Locate every Plasmodium parasite.
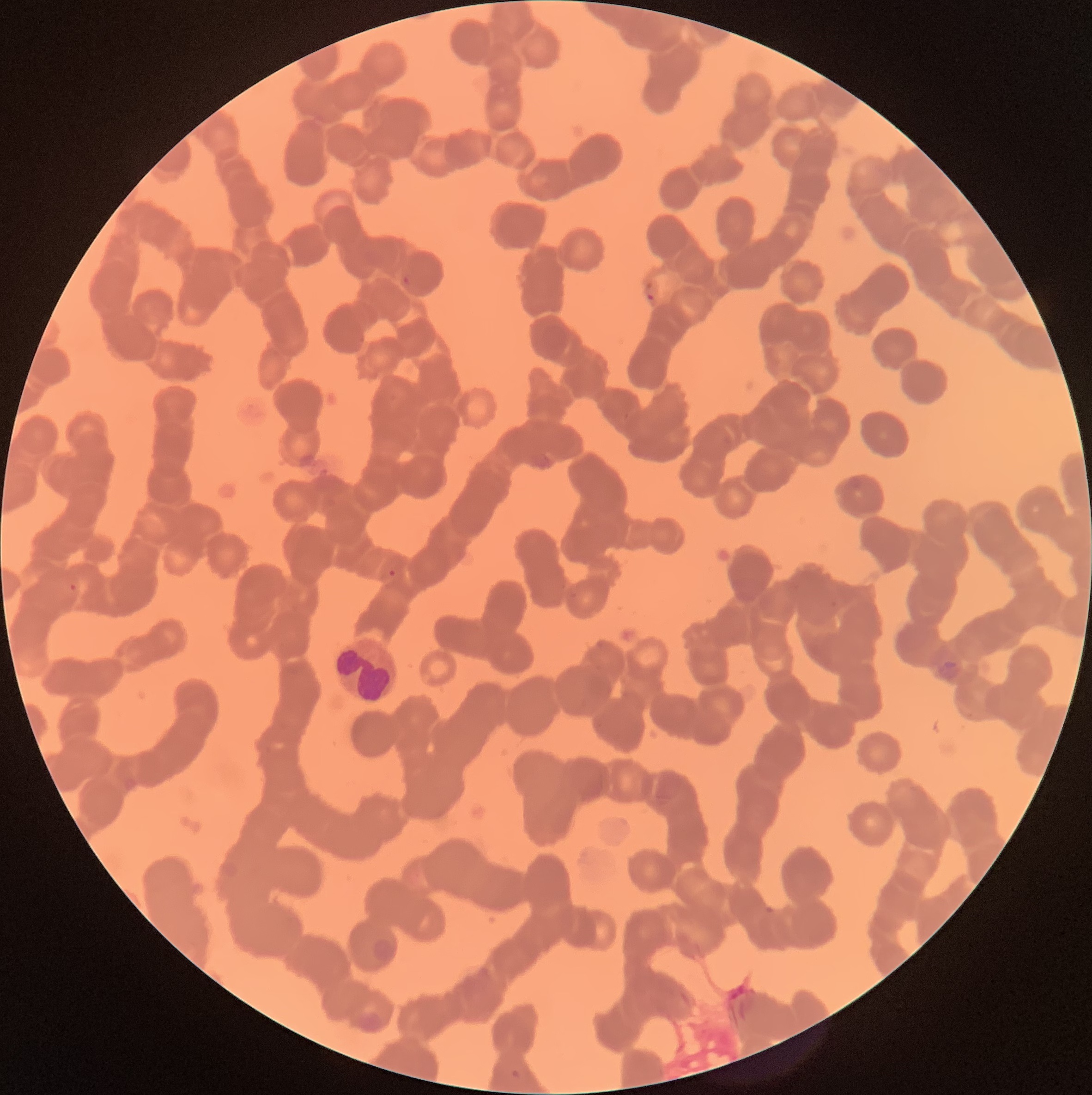
Approximate bounding boxes as [x1, y1, x2, y2] in pixels.
Plasmodium parasites: [401, 273, 412, 287], [643, 280, 655, 302], [387, 568, 397, 578], [68, 582, 77, 593], [936, 659, 961, 681].

Summary:
  - White blood cell locations: [331, 635, 404, 706]
  - Red blood cell morphology: rouleaux formation
  - Image size: 1092×1095 pixels
  - Preparation: thin blood film
  - Modality: optical microscopy